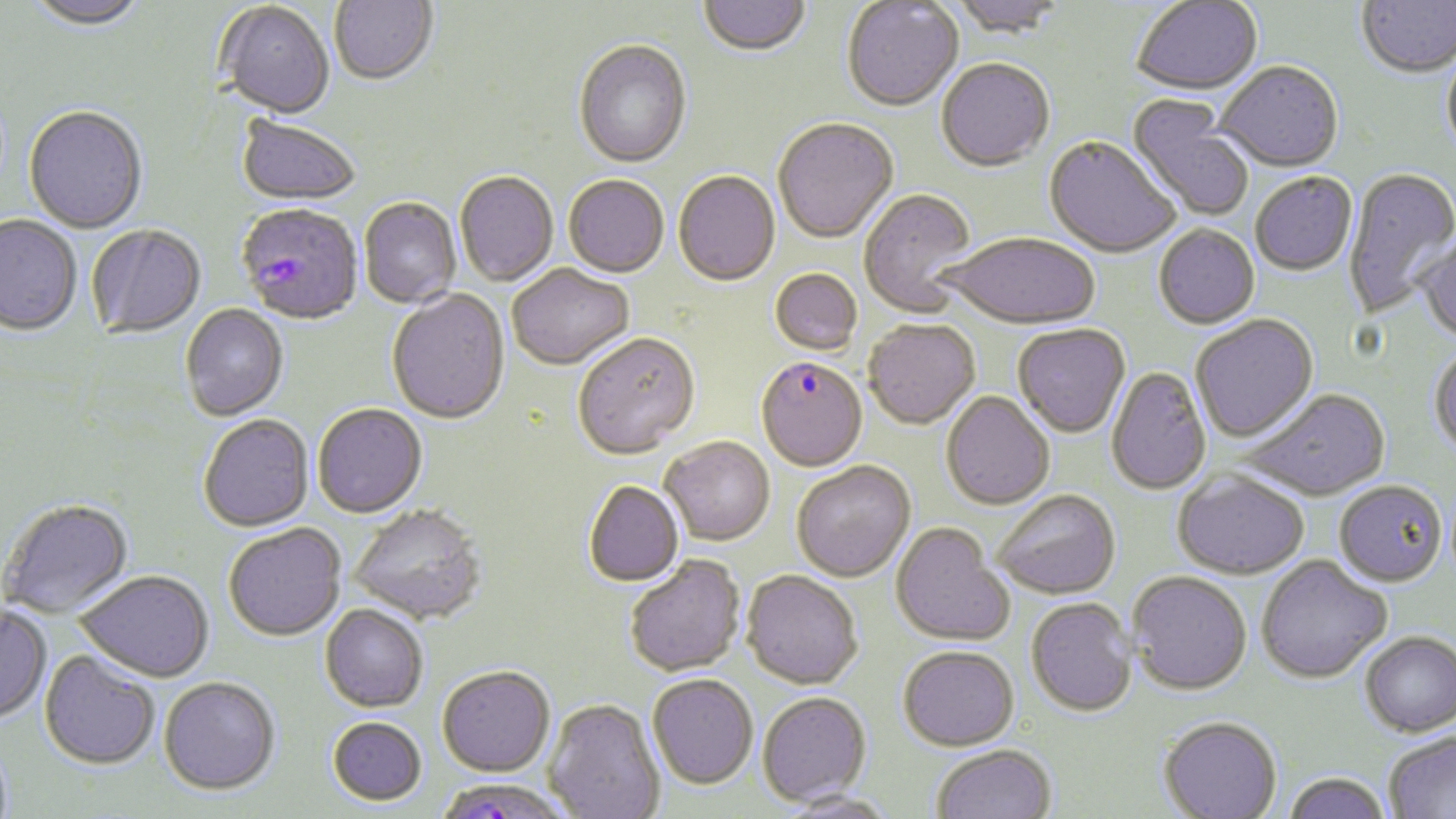
{
  "plasmodium_falciparum_infected_red_blood_cell_locations": "approximate bounding boxes as (x1, y1, x2, y2) in pixels: (237, 206, 364, 328), (756, 357, 868, 473), (433, 777, 574, 819)",
  "slide_level_diagnosis": "Plasmodium falciparum",
  "preparation": "thin blood film",
  "uninfected_red_blood_cell_locations": "approximate bounding boxes as (x1, y1, x2, y2) in pixels: (23, 0, 150, 32), (330, 0, 438, 88), (699, 0, 811, 59), (948, 0, 1066, 42), (1131, 0, 1264, 98), (1357, 0, 1456, 80), (842, 1, 963, 114), (214, 3, 335, 121), (573, 42, 692, 170), (1441, 50, 1456, 163), (936, 61, 1055, 174), (1216, 63, 1343, 175), (1126, 97, 1254, 222), (23, 107, 148, 236), (235, 116, 361, 209), (772, 119, 899, 246), (1044, 137, 1180, 260), (1343, 168, 1456, 320), (454, 173, 558, 288), (673, 173, 780, 288), (1250, 174, 1358, 277), (563, 177, 669, 279), (859, 190, 978, 317), (359, 199, 461, 309), (0, 217, 81, 338), (87, 226, 206, 339), (1153, 226, 1260, 330), (942, 235, 1100, 331), (1416, 235, 1456, 347), (508, 265, 635, 372), (769, 270, 862, 356), (387, 291, 510, 427), (180, 305, 288, 421), (1191, 316, 1319, 444), (863, 320, 981, 431), (1013, 325, 1130, 439), (573, 334, 701, 460), (1428, 347, 1456, 459), (1106, 367, 1212, 496), (1242, 390, 1391, 503), (941, 391, 1055, 511), (312, 404, 427, 518), (198, 415, 315, 532), (660, 437, 775, 546), (791, 462, 916, 582), (1173, 473, 1309, 581), (584, 481, 684, 586), (1333, 483, 1448, 589), (993, 491, 1120, 600), (1, 499, 135, 619), (349, 505, 489, 627), (223, 523, 346, 641), (890, 524, 1014, 647), (625, 555, 746, 677), (1256, 558, 1392, 686), (76, 570, 213, 682), (742, 571, 864, 690), (1127, 573, 1252, 697), (1026, 599, 1138, 719), (320, 603, 428, 711), (0, 606, 52, 724), (1360, 633, 1456, 737), (898, 647, 1019, 752), (40, 650, 160, 770), (437, 665, 555, 776), (647, 674, 758, 789), (158, 676, 280, 795), (757, 692, 872, 805), (544, 698, 665, 819), (327, 717, 427, 805), (1158, 718, 1282, 819), (1383, 732, 1456, 819), (931, 745, 1056, 819), (1282, 773, 1392, 819), (777, 790, 899, 818)",
  "stain": "May-Grünwald-Giemsa",
  "field_of_view": "single",
  "modality": "light microscopy",
  "image_size": "1456×819 pixels",
  "magnification": "1000x"
}